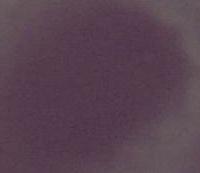 A red blood cell is shown. Photomicrograph. 1000x magnification.